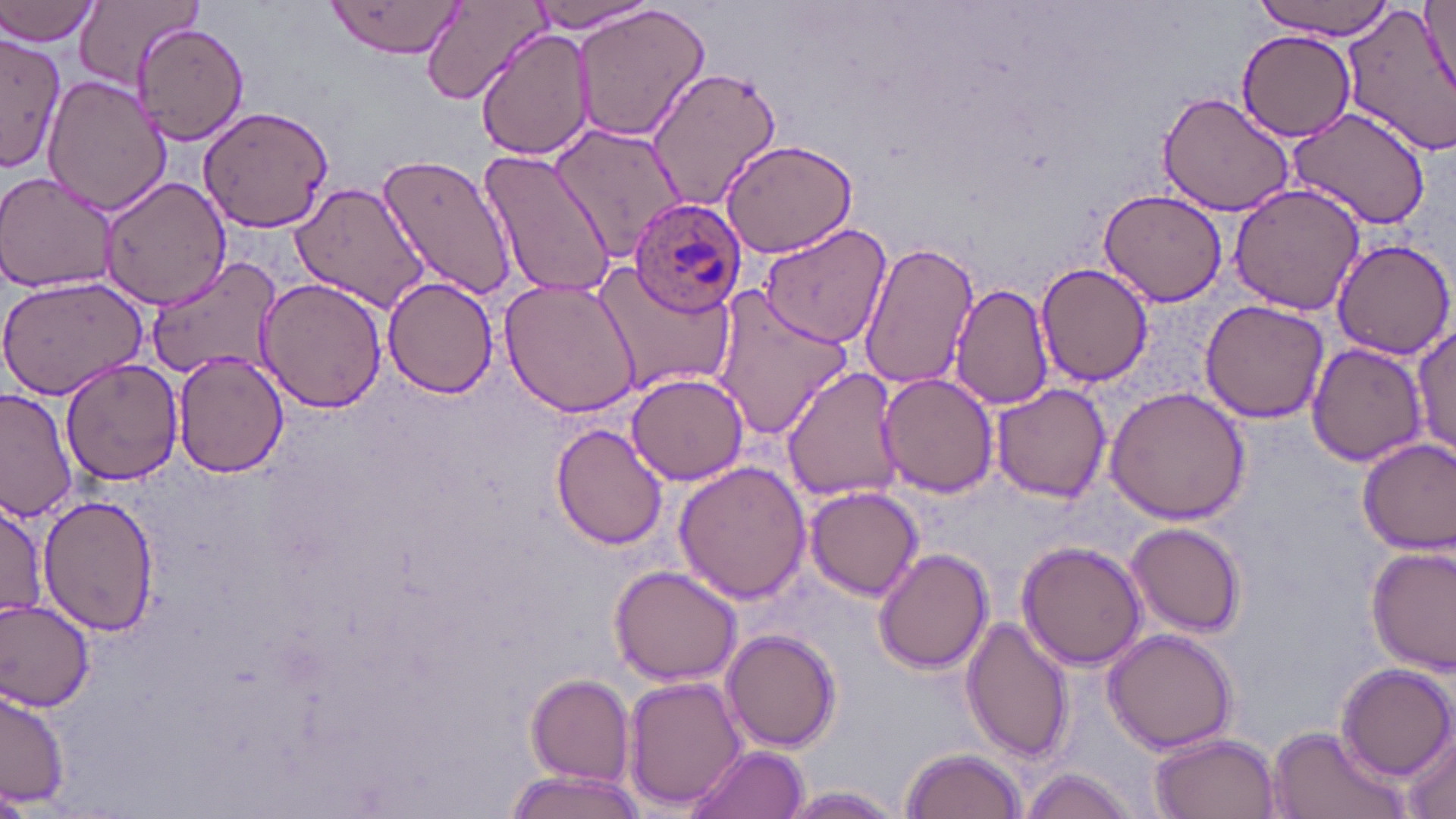

slide-level diagnosis = Plasmodium ovale
uninfected red blood cell locations = approximate bounding boxes as (x1, y1, x2, y2) in pixels: (325, 0, 468, 61), (525, 0, 662, 37), (1249, 0, 1397, 43), (1421, 0, 1456, 101), (0, 1, 104, 47), (72, 1, 201, 94), (1340, 1, 1456, 155), (419, 2, 548, 105), (573, 4, 709, 144), (132, 20, 249, 144), (476, 27, 597, 163), (1239, 29, 1354, 142), (0, 35, 69, 171), (646, 63, 784, 211), (42, 74, 172, 216), (1156, 90, 1297, 218), (198, 106, 335, 232), (1289, 108, 1431, 229), (551, 123, 681, 262), (719, 139, 860, 258), (481, 147, 617, 299), (376, 148, 517, 302), (0, 173, 119, 294), (96, 174, 232, 311), (1228, 183, 1368, 316), (291, 184, 429, 313), (1099, 188, 1227, 309), (759, 221, 891, 348), (858, 239, 980, 390), (1330, 239, 1454, 358), (151, 257, 285, 383), (593, 258, 736, 392), (1034, 263, 1155, 387), (0, 276, 149, 402), (381, 277, 499, 397), (501, 277, 641, 416), (255, 278, 386, 414), (951, 281, 1056, 416), (710, 287, 855, 441), (1199, 298, 1329, 424), (1412, 325, 1454, 460), (1307, 343, 1428, 467), (172, 351, 290, 479), (62, 358, 183, 486), (781, 365, 906, 503), (627, 372, 751, 486), (877, 372, 998, 498), (991, 383, 1111, 503), (1105, 384, 1250, 525), (1, 389, 76, 525), (551, 425, 668, 551), (1356, 436, 1456, 557), (672, 460, 811, 604), (805, 485, 924, 600), (36, 492, 160, 638), (0, 503, 50, 621), (1125, 523, 1247, 637), (1018, 539, 1150, 670), (1367, 544, 1455, 674), (872, 549, 993, 675), (607, 565, 742, 685), (0, 600, 96, 711), (961, 615, 1072, 764), (1103, 626, 1241, 754), (724, 630, 839, 753), (1334, 662, 1454, 783), (623, 674, 746, 813), (525, 675, 635, 785), (0, 686, 73, 811), (1265, 722, 1409, 819), (1398, 730, 1456, 819), (1149, 732, 1280, 818), (684, 743, 808, 819), (899, 747, 1027, 819), (1018, 766, 1140, 819), (501, 768, 647, 819), (0, 786, 39, 819), (783, 787, 906, 817)
Plasmodium ovale-infected red blood cell locations = approximate bounding boxes as (x1, y1, x2, y2) in pixels: (627, 201, 748, 314)
image size = 1456×819 pixels
magnification = 1000x
preparation = thin blood smear
field of view = single
stain = May-Grünwald-Giemsa
modality = optical microscopy